Identify the cell.
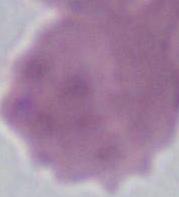
This is an erythrocyte.

Photomicrograph. 1000x magnification.